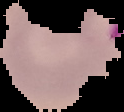 Result: malaria parasites detected. The area outside the segmented cell region is set to black. Image is 124×112 pixels. From a thin blood film.